Locate the cells, classifying each as a parasitized red blood cell, an uninfected red blood cell, or a white blood cell.
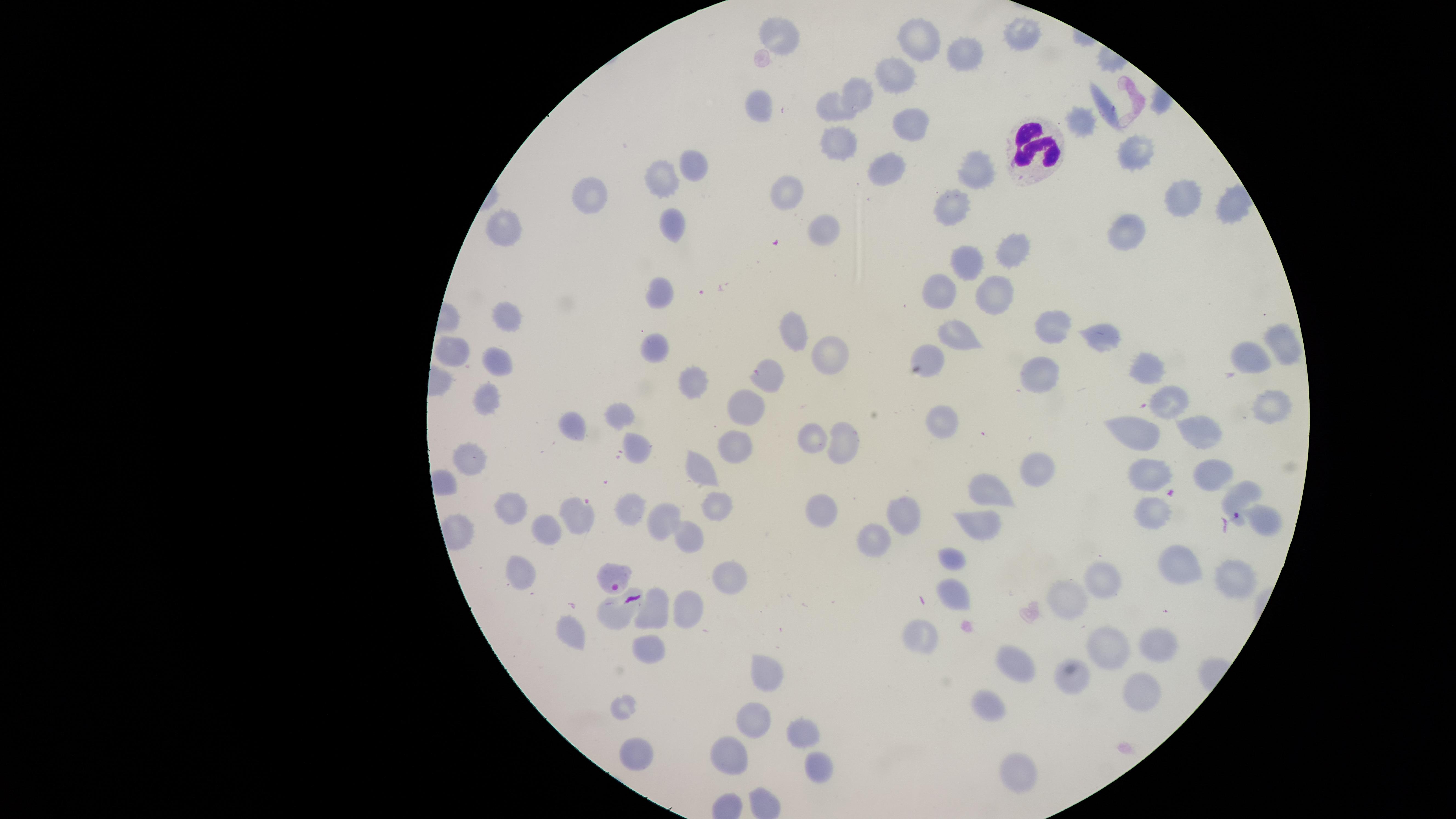
Approximate marker points, in pixels from the top-left corner.
Parasitized red blood cells: (x=1241, y=493), (x=615, y=578).
Uninfected red blood cells: (x=785, y=28), (x=920, y=37), (x=1022, y=37), (x=961, y=52), (x=894, y=74), (x=859, y=92), (x=830, y=97), (x=1098, y=103), (x=756, y=108), (x=910, y=123), (x=1085, y=123), (x=839, y=139), (x=1134, y=152), (x=692, y=163), (x=883, y=165), (x=981, y=172), (x=665, y=174), (x=789, y=190), (x=591, y=193), (x=1179, y=195), (x=1230, y=208), (x=947, y=209), (x=504, y=227), (x=671, y=227), (x=822, y=229), (x=1135, y=232), (x=1017, y=251), (x=975, y=266), (x=940, y=288), (x=661, y=295), (x=998, y=298), (x=517, y=316), (x=1051, y=318), (x=795, y=328), (x=955, y=336), (x=1108, y=337), (x=1283, y=344), (x=654, y=347), (x=833, y=349), (x=454, y=352), (x=930, y=353), (x=1247, y=360), (x=498, y=363), (x=1042, y=369), (x=1150, y=374), (x=763, y=377), (x=697, y=385), (x=486, y=396), (x=1169, y=403), (x=1268, y=409), (x=618, y=410), (x=744, y=410), (x=946, y=421), (x=574, y=427), (x=1136, y=432), (x=1206, y=433), (x=814, y=435), (x=849, y=436), (x=734, y=445), (x=638, y=450), (x=472, y=458), (x=1030, y=468), (x=703, y=470), (x=1148, y=472), (x=1213, y=472), (x=985, y=499), (x=717, y=505), (x=509, y=508), (x=625, y=509), (x=904, y=512), (x=1155, y=512), (x=578, y=513), (x=824, y=513), (x=666, y=518), (x=1262, y=524), (x=976, y=529), (x=549, y=532), (x=686, y=532), (x=869, y=533), (x=952, y=557), (x=1179, y=566), (x=517, y=572), (x=722, y=573), (x=1105, y=578), (x=1236, y=580), (x=954, y=592), (x=1067, y=598), (x=687, y=603), (x=650, y=608), (x=615, y=609), (x=573, y=631), (x=919, y=633), (x=644, y=645), (x=1160, y=647), (x=1104, y=649), (x=1013, y=661), (x=772, y=670), (x=1074, y=675), (x=1137, y=695), (x=990, y=705), (x=749, y=721), (x=799, y=728), (x=734, y=751), (x=1010, y=755), (x=638, y=758), (x=822, y=769).
White blood cells: (x=1032, y=147).

Circular visible region. Smartphone photograph through the microscope eyepiece. Image is 1456×819 pixels. Single field of view. Species: Plasmodium falciparum. Thin blood smear. Giemsa-stained preparation.